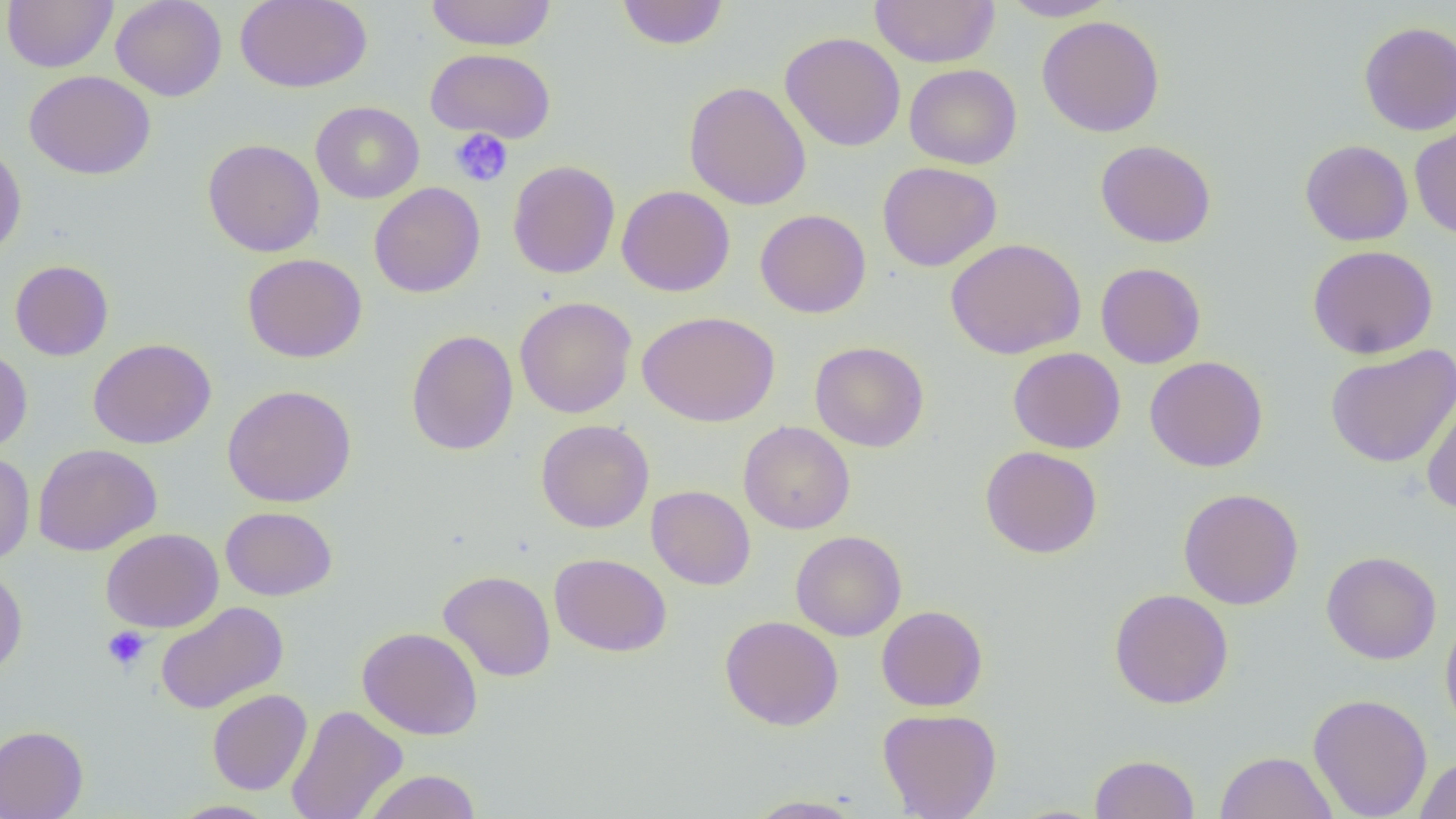
Approximate bounding boxes as named x1/y1/x2/y2 corners in pixels. Uninfected red blood cell locations: (x1=2, y1=0, x2=118, y2=73), (x1=111, y1=0, x2=227, y2=101), (x1=235, y1=0, x2=372, y2=93), (x1=425, y1=0, x2=557, y2=51), (x1=869, y1=0, x2=1000, y2=68), (x1=1001, y1=0, x2=1119, y2=21), (x1=616, y1=1, x2=729, y2=50), (x1=1037, y1=15, x2=1165, y2=138), (x1=1359, y1=21, x2=1456, y2=135), (x1=779, y1=31, x2=906, y2=152), (x1=426, y1=48, x2=556, y2=143), (x1=905, y1=64, x2=1021, y2=169), (x1=24, y1=70, x2=156, y2=180), (x1=684, y1=80, x2=812, y2=210), (x1=311, y1=101, x2=424, y2=203), (x1=1409, y1=122, x2=1456, y2=240), (x1=202, y1=139, x2=324, y2=257), (x1=1299, y1=139, x2=1413, y2=246), (x1=1096, y1=140, x2=1216, y2=247), (x1=0, y1=143, x2=27, y2=259), (x1=508, y1=160, x2=620, y2=278), (x1=877, y1=161, x2=1003, y2=272), (x1=369, y1=182, x2=485, y2=298), (x1=617, y1=185, x2=735, y2=297), (x1=755, y1=209, x2=871, y2=318), (x1=945, y1=238, x2=1085, y2=359), (x1=1307, y1=244, x2=1438, y2=359), (x1=242, y1=253, x2=368, y2=363), (x1=10, y1=260, x2=114, y2=361), (x1=1095, y1=262, x2=1206, y2=368), (x1=514, y1=296, x2=636, y2=418), (x1=637, y1=311, x2=780, y2=427), (x1=406, y1=329, x2=519, y2=455), (x1=88, y1=337, x2=216, y2=449), (x1=810, y1=341, x2=929, y2=452), (x1=1325, y1=345, x2=1456, y2=468), (x1=1008, y1=347, x2=1126, y2=454), (x1=0, y1=348, x2=33, y2=453), (x1=1145, y1=356, x2=1268, y2=473), (x1=223, y1=384, x2=357, y2=507), (x1=1421, y1=385, x2=1456, y2=516), (x1=535, y1=419, x2=654, y2=533), (x1=739, y1=421, x2=855, y2=534), (x1=33, y1=443, x2=162, y2=555), (x1=980, y1=445, x2=1102, y2=558), (x1=0, y1=451, x2=35, y2=564), (x1=646, y1=485, x2=755, y2=590), (x1=1178, y1=488, x2=1304, y2=610), (x1=221, y1=506, x2=337, y2=601), (x1=101, y1=528, x2=223, y2=632), (x1=791, y1=530, x2=906, y2=641), (x1=1321, y1=551, x2=1442, y2=664), (x1=549, y1=552, x2=672, y2=657), (x1=0, y1=566, x2=28, y2=678), (x1=438, y1=570, x2=556, y2=681), (x1=1109, y1=588, x2=1234, y2=709), (x1=155, y1=601, x2=288, y2=714), (x1=876, y1=605, x2=988, y2=711), (x1=1440, y1=612, x2=1456, y2=738), (x1=720, y1=615, x2=844, y2=731), (x1=357, y1=627, x2=484, y2=739), (x1=207, y1=689, x2=312, y2=795), (x1=1308, y1=693, x2=1433, y2=819), (x1=286, y1=705, x2=408, y2=819), (x1=878, y1=708, x2=1002, y2=819), (x1=0, y1=725, x2=88, y2=819), (x1=1215, y1=750, x2=1337, y2=819), (x1=1090, y1=754, x2=1199, y2=818), (x1=1414, y1=756, x2=1456, y2=818), (x1=362, y1=770, x2=482, y2=819), (x1=744, y1=795, x2=867, y2=818), (x1=167, y1=800, x2=278, y2=819). Platelet locations: (x1=450, y1=128, x2=513, y2=187), (x1=102, y1=626, x2=151, y2=671). Slide-level diagnosis: negative for blood parasites. 1000x magnification. Optical microscopy. Thin blood film. Single field of view. Image is 1456×819 pixels.